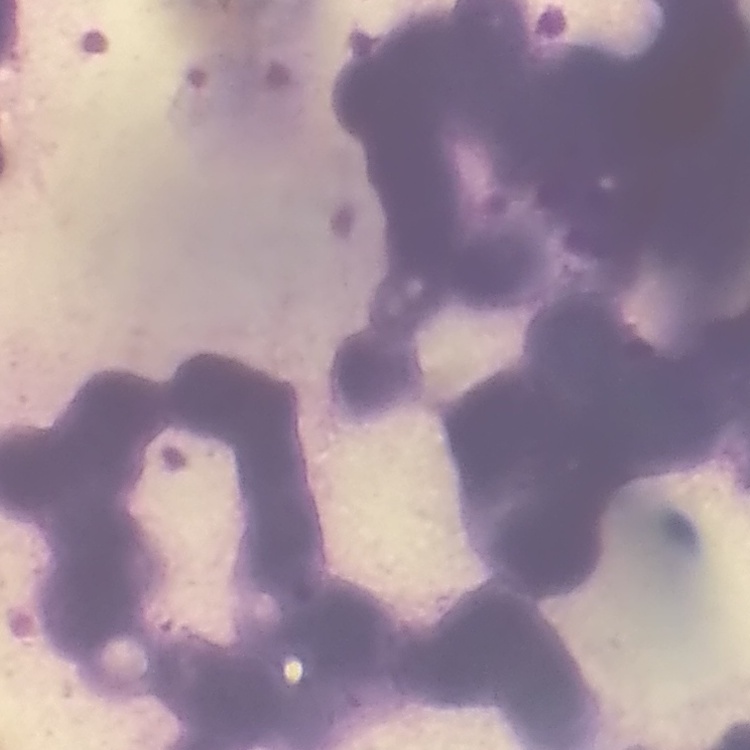

Summary:
  - Red blood cell morphology: rouleaux formation
  - Stain: Field's or Giemsa
  - Preparation: thin peripheral smear
  - Image type: one tile cut from a larger photomicrograph